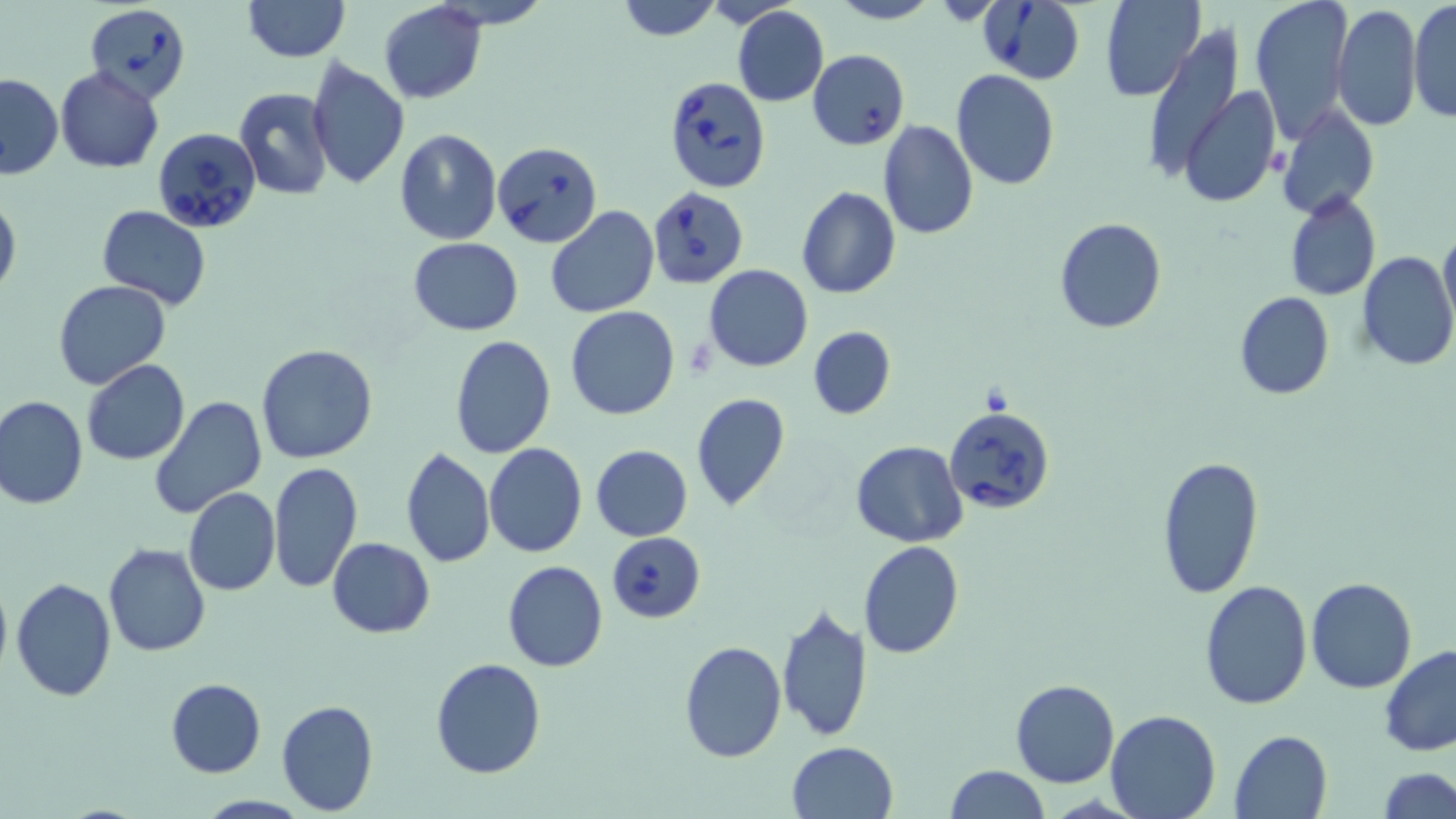 Approximate bounding boxes as (x1,y1)-(x2,y2) corner pairs in pixels. Uninfected red blood cell locations: (240,0)-(351,64), (615,0)-(723,41), (829,0)-(938,26), (1247,0)-(1354,140), (1408,0)-(1455,123), (378,1)-(487,104), (1099,1)-(1205,101), (731,6)-(829,107), (1331,6)-(1421,133), (1143,27)-(1243,188), (306,60)-(409,189), (55,66)-(164,173), (951,69)-(1061,190), (0,72)-(62,179), (232,87)-(335,200), (1179,87)-(1281,206), (1277,106)-(1380,218), (878,119)-(979,239), (395,128)-(501,244), (796,186)-(901,300), (0,189)-(21,302), (1284,191)-(1381,301), (96,205)-(212,309), (545,207)-(660,319), (1053,217)-(1168,334), (1439,226)-(1456,333), (410,238)-(523,335), (1357,251)-(1455,371), (705,264)-(813,371), (52,280)-(170,390), (1234,291)-(1335,399), (566,306)-(679,420), (808,326)-(896,419), (449,336)-(557,458), (257,344)-(378,465), (82,360)-(190,467), (691,393)-(790,512), (1,394)-(89,509), (150,396)-(267,520), (850,441)-(967,547), (484,443)-(587,560), (589,445)-(693,541), (401,446)-(495,569), (1156,453)-(1264,598), (268,462)-(363,593), (183,487)-(280,596), (327,537)-(436,638), (861,540)-(965,658), (103,542)-(212,657), (503,561)-(607,672), (10,577)-(116,702), (1305,577)-(1417,693), (1198,580)-(1313,711), (776,604)-(873,742), (679,639)-(787,762), (1379,644)-(1456,758), (430,657)-(547,780), (165,678)-(266,777), (1010,678)-(1121,788), (276,699)-(380,815), (1104,711)-(1220,819), (1230,730)-(1333,819), (786,741)-(899,819), (942,763)-(1048,819), (1379,767)-(1456,819). Babesia divergens-infected red blood cell locations: (979,0)-(1086,85), (83,2)-(192,102), (807,49)-(909,150), (664,76)-(772,193), (155,128)-(263,230), (493,141)-(602,247), (651,186)-(752,289), (944,405)-(1056,512), (606,530)-(705,622). Slide-level diagnosis: Babesia divergens. May-Grünwald-Giemsa-stained preparation. Light microscopy. Captured at 1000x magnification. Thin blood smear. One field of a larger specimen. Image is 1456×819 pixels.